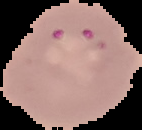

Summary:
  - Image size: 142×130 pixels
  - Image type: segmented cell region on a black background
  - Preparation: thin blood smear
  - Malaria status: parasitized